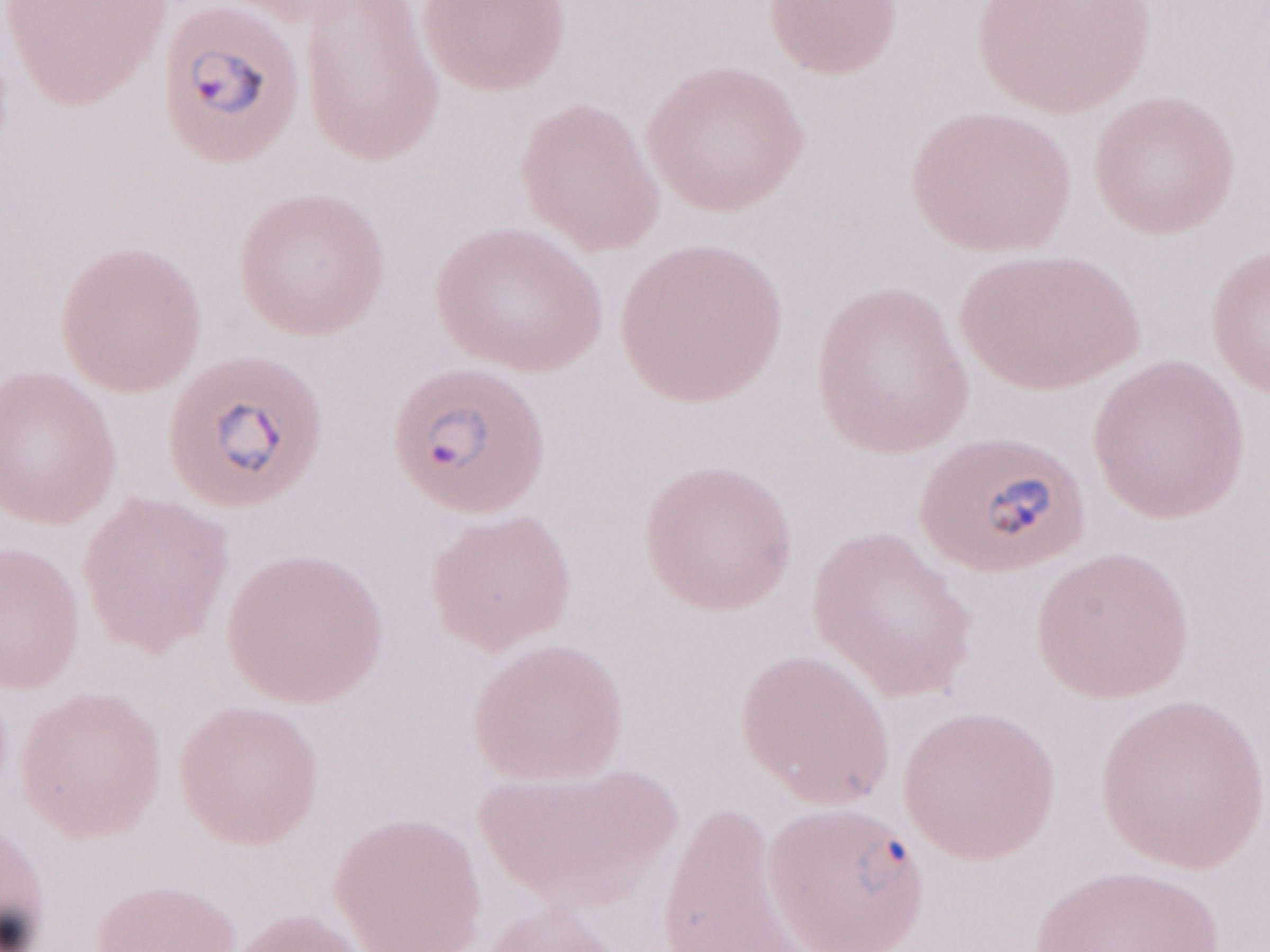 Malaria diagnosis (patient-level): positive. Image is 1270×952 pixels. Single field of view. Magnification: 1,000x. Olympus BX43 microscope and DP73 digital camera. May-Grünwald-Giemsa stain. Thin blood film.